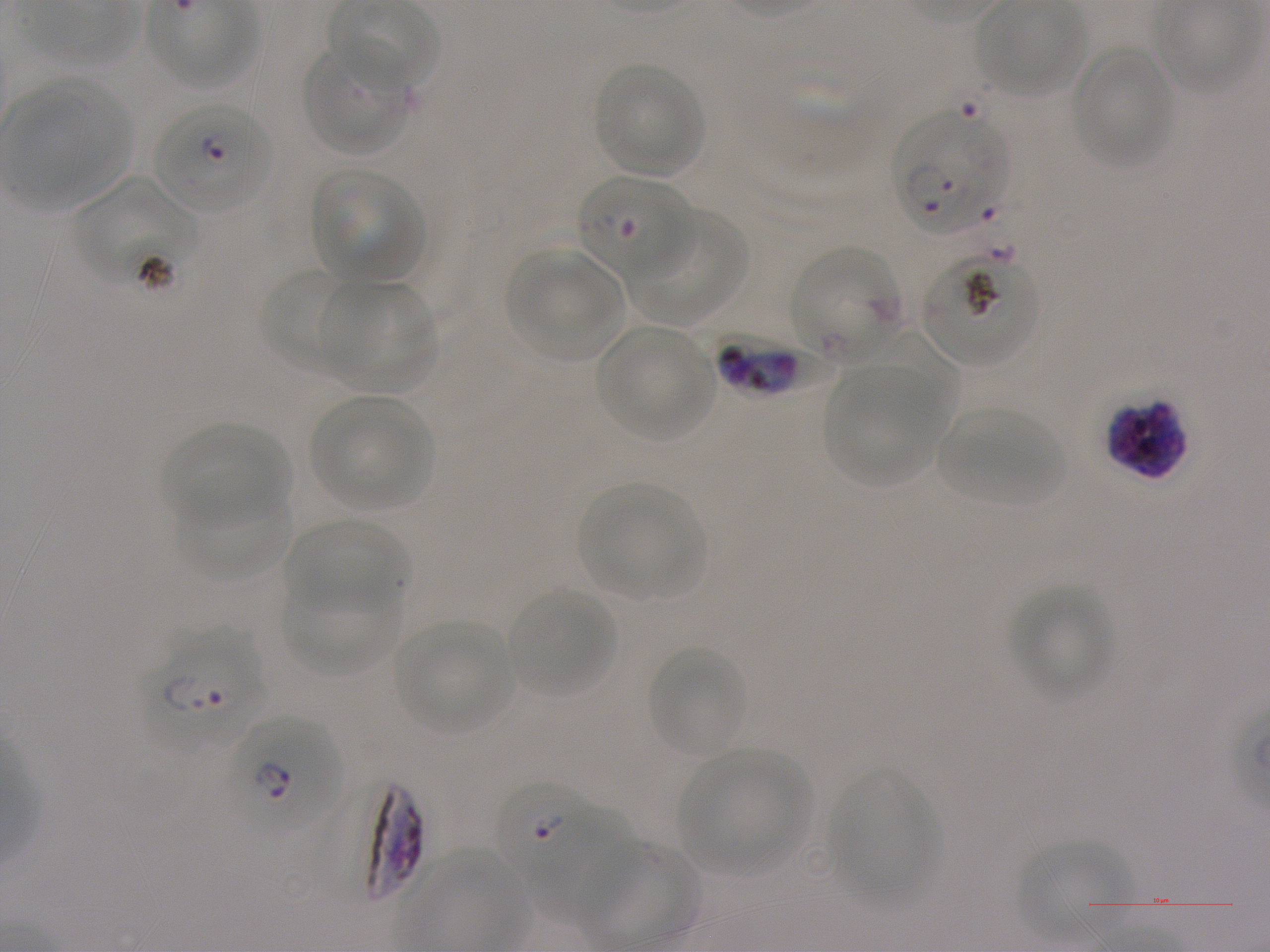

Approximate bounding boxes as {x1, y1, x2, y2} in pixels. Not every red blood cell is marked. A life-cycle stage — or a range of stages, where the recorded stages span more than one — follows each staged infected red blood cell.
Summary:
  - Locations of uninfected red blood cells: {978, 0, 1083, 97}, {304, 42, 412, 155}, {1073, 45, 1172, 168}, {594, 63, 705, 176}, {312, 168, 424, 281}, {74, 177, 202, 288}, {627, 212, 748, 325}, {507, 248, 622, 358}, {259, 269, 362, 375}, {326, 280, 438, 392}, {597, 325, 714, 440}, {845, 329, 959, 425}, {824, 370, 943, 484}, {311, 395, 433, 510}, {937, 407, 1065, 506}, {160, 423, 292, 525}, {578, 483, 705, 599}, {175, 485, 293, 582}, {285, 519, 409, 611}, {281, 572, 402, 674}, {1009, 583, 1113, 700}, {507, 587, 616, 697}, {394, 621, 513, 734}, {648, 647, 748, 758}, {680, 748, 810, 875}, {829, 768, 939, 906}, {533, 813, 632, 923}, {1017, 841, 1136, 943}
  - Locations of infected red blood cells: {155, 103, 272, 212} early ring; {790, 247, 901, 363}; {705, 331, 832, 399}; {1106, 398, 1187, 480}; {144, 628, 266, 748} ring; {229, 716, 341, 833} early ring to early trophozoite; {304, 781, 425, 907}; {496, 782, 596, 884} ring
  - Locations of red blood cells of indeterminate infection status: {892, 112, 1006, 236}, {577, 175, 693, 281}, {923, 251, 1038, 366}
  - Preparation: thin blood film
  - Stain: Giemsa
  - Donor blood group: A+
  - Image size: 1270×952 pixels
  - Field of view: single
  - Objective: 100x, oil immersion, numerical aperture 1.25
  - Culture: P. falciparum strain NF54, static, in vitro